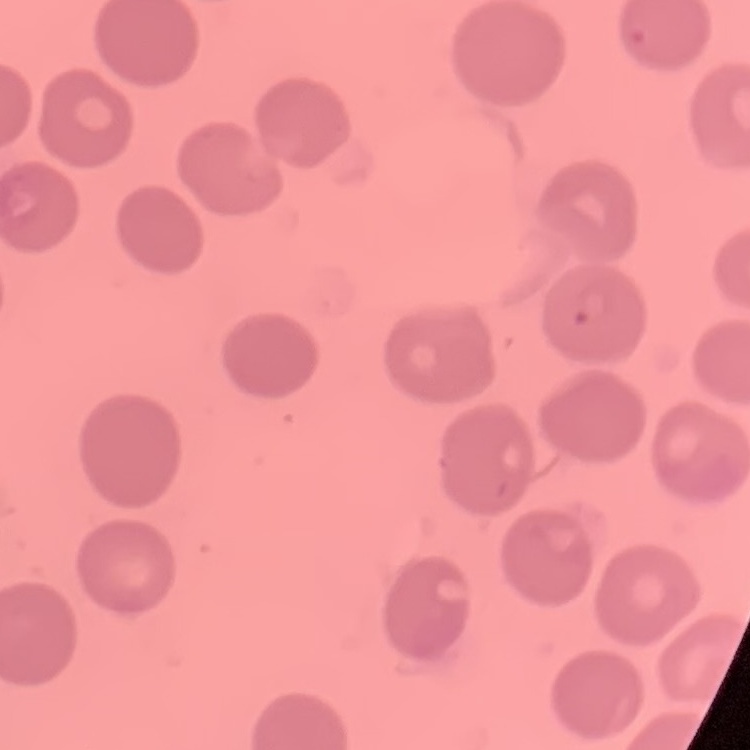

{
  "erythrocyte_morphology": "no rouleaux formation",
  "stain": "Field's or Giemsa",
  "image_type": "one tile cut from a larger photomicrograph",
  "preparation": "thin peripheral smear"
}